Outline each blood parasite and name the species.
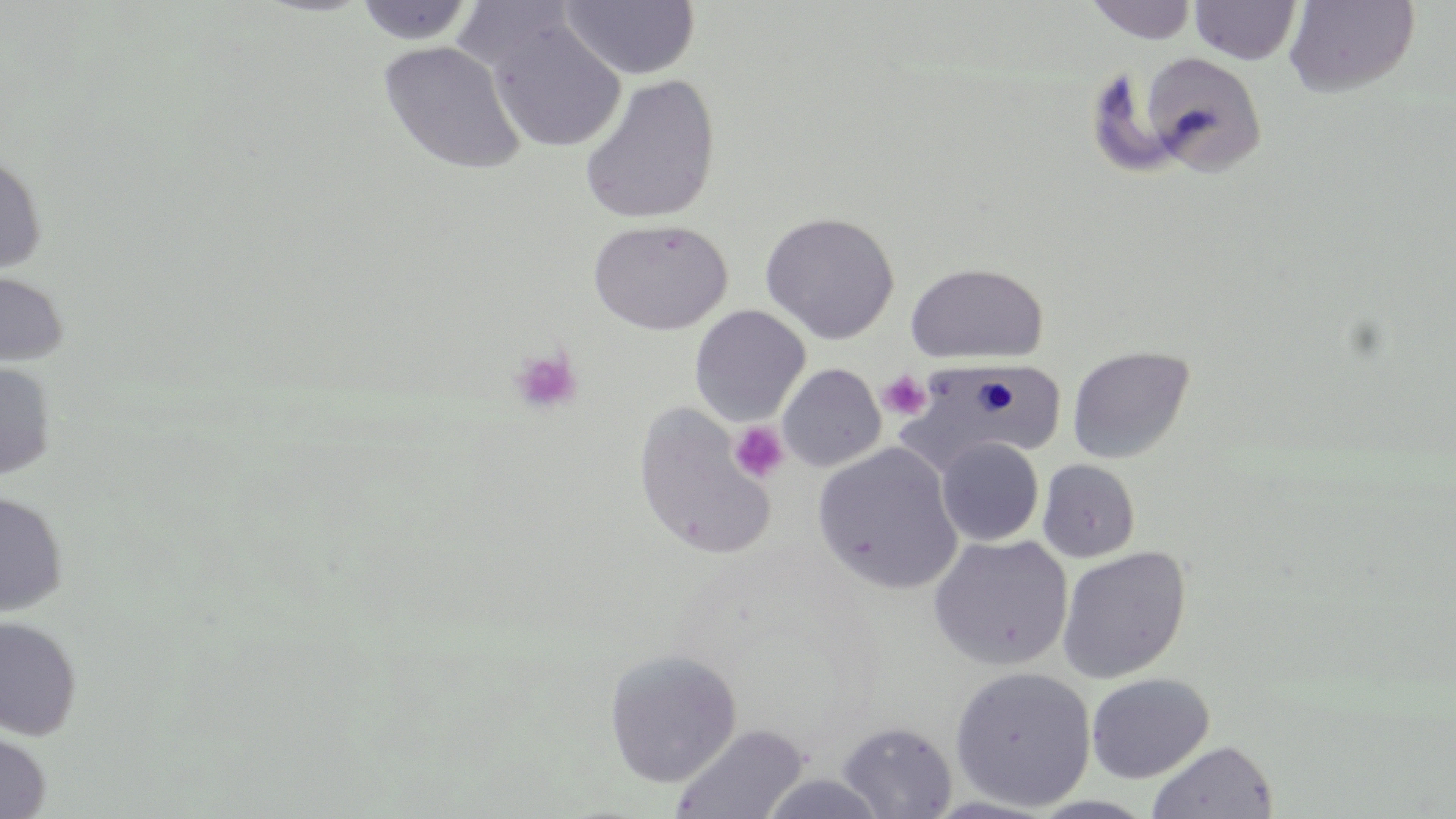
No blood parasites observed.

slide-level diagnosis = no evidence of blood parasites
image size = 1456×819 pixels
stain = May-Grünwald-Giemsa
uninfected red blood cell locations = approximate bounding boxes as (x1, y1, x2, y2) in pixels: (560, 0, 700, 80), (1085, 0, 1198, 43), (1285, 0, 1419, 96), (354, 1, 477, 45), (1190, 1, 1301, 64), (485, 15, 625, 153), (377, 40, 526, 175), (1139, 52, 1267, 177), (578, 75, 721, 225), (0, 154, 47, 274), (761, 211, 900, 343), (588, 218, 733, 335), (906, 262, 1048, 365), (0, 272, 69, 367), (689, 305, 811, 426), (1066, 345, 1195, 464), (900, 361, 1066, 475), (0, 362, 57, 480), (777, 363, 886, 472), (632, 404, 778, 561), (936, 437, 1044, 546), (812, 444, 962, 595), (1038, 459, 1141, 563), (0, 492, 67, 617), (928, 534, 1074, 671), (1056, 546, 1191, 684), (0, 616, 83, 741), (603, 649, 742, 787), (949, 666, 1096, 811), (1086, 673, 1214, 783), (837, 721, 957, 818), (670, 723, 809, 819), (0, 731, 51, 818), (1147, 739, 1278, 819), (759, 772, 890, 818)
modality = light microscopy
magnification = 1000x
preparation = thin blood film
platelet locations = approximate bounding boxes as (x1, y1, x2, y2) in pixels: (509, 346, 583, 416), (877, 369, 931, 419), (728, 421, 790, 484)
field of view = one of a larger specimen